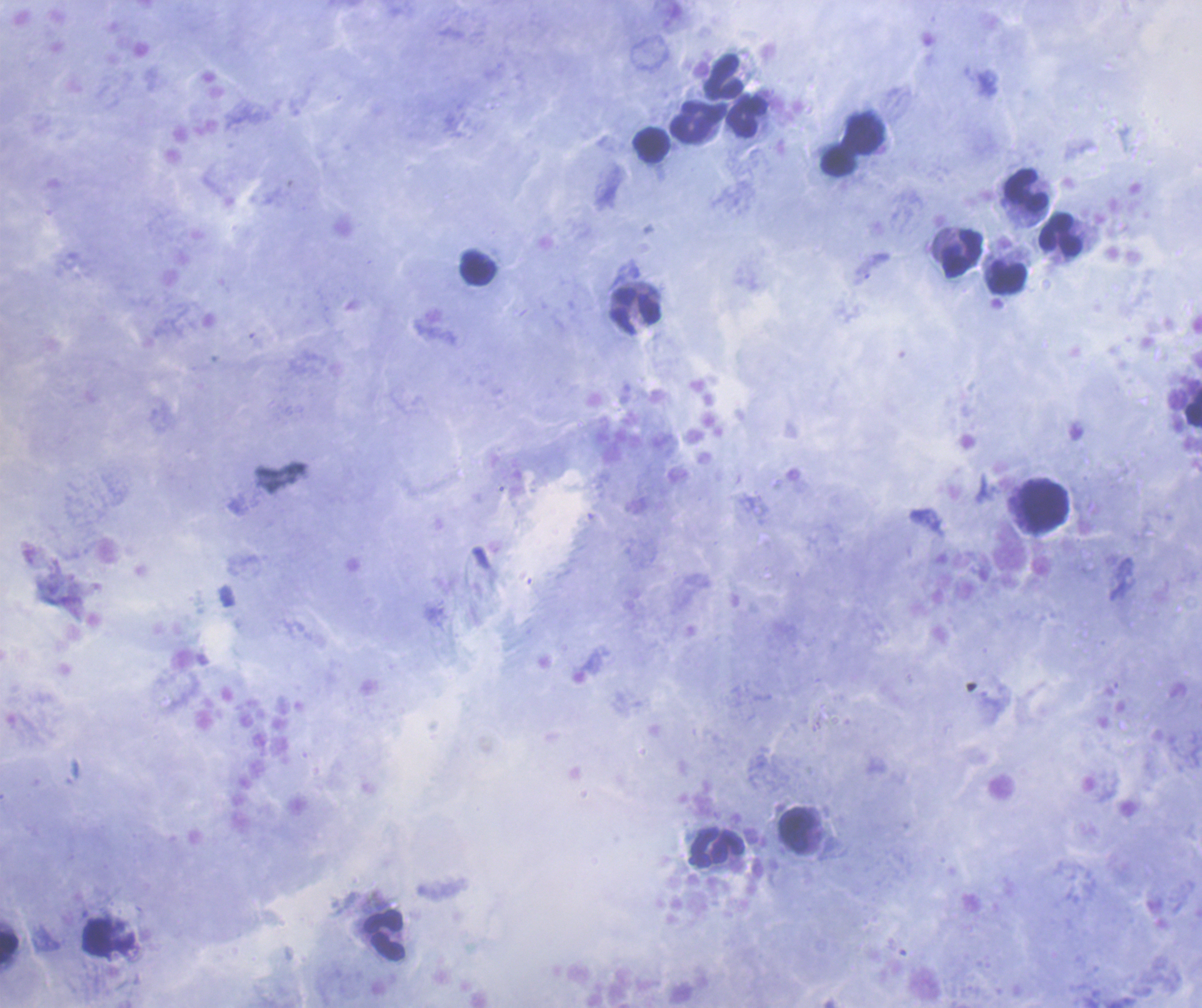
{
  "background_quality": "good",
  "preparation": "thick smear of blood",
  "magnification": "100x",
  "stain": "Romanowsky",
  "coloration_quality": "good",
  "image_size": "1202×1008 pixels",
  "context": "previously used in an actual diagnosis",
  "result": "no malaria parasites seen",
  "field_of_view": "one from this slide",
  "leukocyte_locations": "approximate centers as (x, y) in pixels: (724, 77), (748, 117), (695, 123), (867, 134), (652, 145), (838, 161), (1026, 192), (1061, 235), (961, 252), (478, 268), (1006, 279), (634, 310), (1194, 407), (1044, 506), (797, 831), (717, 848), (385, 935), (9, 948)"
}